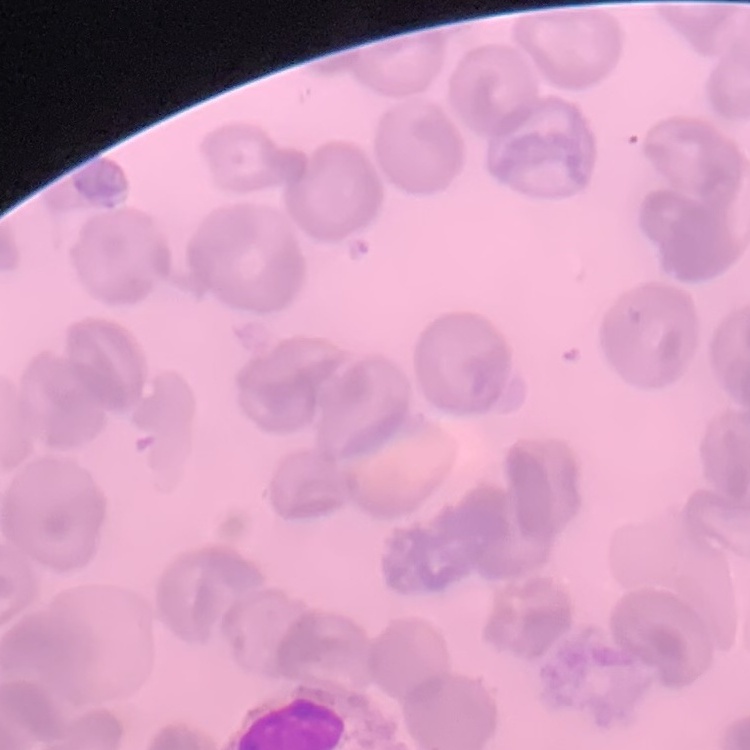
The erythrocytes show no rouleaux formation. One tile cut from a larger photomicrograph. Field's or Giemsa stain. Thin peripheral smear.